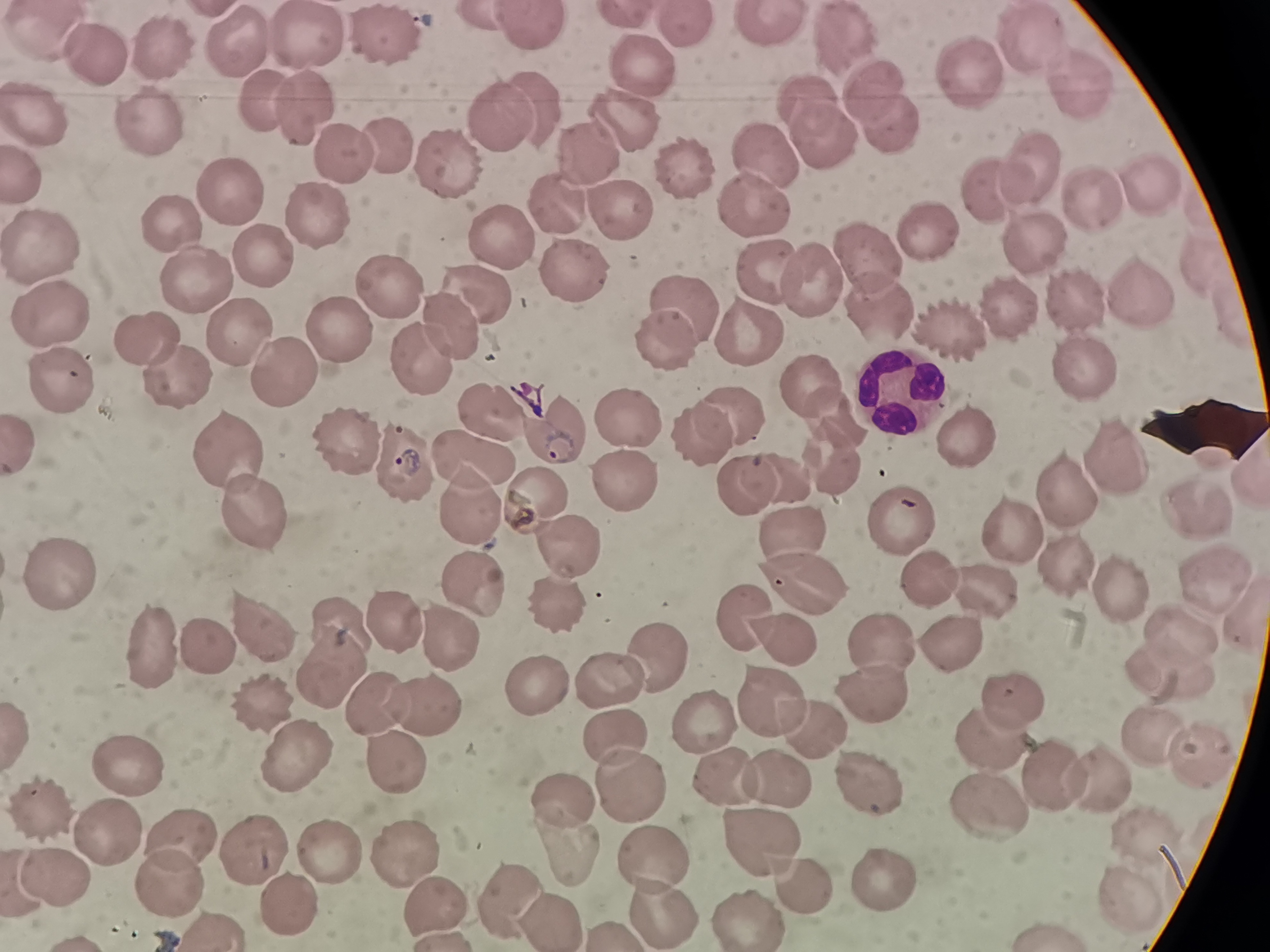
Approximate centers as {x, y} in pixels. Cell locations: {769, 25}, {682, 28}, {531, 30}, {46, 35}, {243, 36}, {308, 39}, {840, 41}, {1028, 41}, {387, 43}, {161, 49}, {96, 62}, {644, 69}, {1071, 79}, {961, 80}, {869, 97}, {261, 99}, {803, 100}, {536, 103}, {306, 104}, {495, 113}, {44, 115}, {886, 123}, {628, 125}, {153, 128}, {815, 138}, {401, 145}, {591, 153}, {349, 158}, {758, 158}, {447, 165}, {1032, 166}, {26, 170}, {683, 178}, {1093, 190}, {988, 191}, {230, 196}, {1148, 196}, {557, 205}, {319, 209}, {611, 213}, {748, 213}, {180, 224}, {922, 231}, {1028, 239}, {503, 241}, {44, 246}, {259, 249}, {865, 255}, {1201, 263}, {564, 271}, {764, 273}, {806, 276}, {200, 279}, {390, 288}, {473, 289}, {1132, 289}, {874, 303}, {1075, 306}, {682, 307}, {50, 316}, {1008, 318}, {334, 323}, {954, 323}, {448, 328}, {746, 330}, {145, 332}, {245, 338}, {661, 345}, {407, 368}, {286, 373}, {59, 376}, {1088, 377}, {182, 380}, {807, 381}, {892, 401}, {494, 410}, {738, 416}, {833, 417}, {623, 423}, {699, 434}, {567, 435}, {343, 446}, {962, 446}, {479, 456}, {227, 457}, {1113, 457}, {401, 467}, {834, 467}, {1244, 469}, {742, 478}, {791, 479}, {1059, 487}, {615, 492}, {538, 501}, {1197, 509}, {468, 510}, {255, 518}, {892, 526}, {1017, 529}, {799, 530}, {566, 552}, {57, 575}, {807, 575}, {1067, 575}, {922, 578}, {471, 582}, {1208, 582}, {986, 597}, {1117, 597}, {553, 604}, {745, 613}, {396, 620}, {266, 629}, {453, 629}, {1175, 633}, {787, 634}, {876, 643}, {945, 646}, {207, 649}, {149, 650}, {654, 653}, {334, 664}, {1165, 675}, {601, 680}, {528, 687}, {1009, 695}, {420, 699}, {763, 701}, {869, 704}, {271, 706}, {807, 725}, {614, 729}, {713, 733}, {984, 737}, {1143, 739}, {390, 750}, {1189, 754}, {298, 755}, {134, 764}, {777, 776}, {623, 778}, {868, 779}, {1089, 780}, {725, 782}, {1050, 785}, {560, 802}, {48, 805}, {983, 805}, {110, 830}, {1143, 831}, {555, 838}, {753, 838}, {182, 842}, {257, 845}, {328, 846}, {400, 851}, {647, 858}, {57, 869}, {794, 877}, {893, 877}, {163, 881}, {1120, 889}, {500, 891}, {429, 895}, {540, 907}, {666, 908}, {748, 916}. Giemsa-stained preparation. Single field of view. Image is 1270×952 pixels. Thin blood film. Photographed with a smartphone camera at the microscope eyepiece.